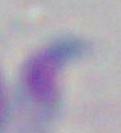

Toxoplasma gondii is seen. 1000x magnification. Micrograph.